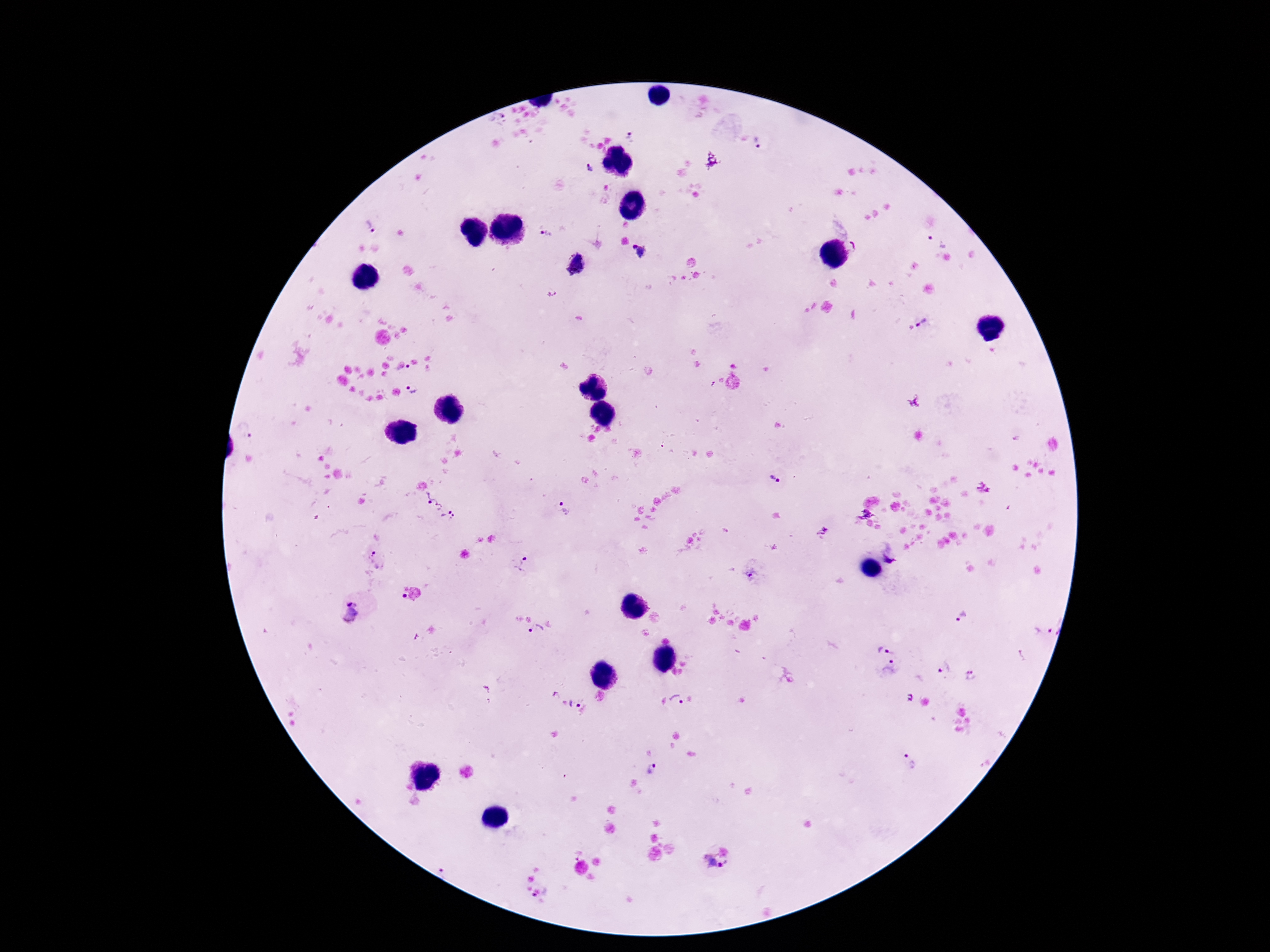

Approximate object centers, in pixels from the top-left corner. Plasmodium parasite locations: (x=632, y=136), (x=759, y=143), (x=590, y=167), (x=371, y=226), (x=546, y=233), (x=938, y=241), (x=855, y=246), (x=643, y=252), (x=575, y=264), (x=922, y=321), (x=409, y=366), (x=413, y=391), (x=247, y=429), (x=775, y=480), (x=435, y=501), (x=563, y=510), (x=449, y=518), (x=822, y=530), (x=378, y=559), (x=524, y=565), (x=751, y=574), (x=403, y=595), (x=351, y=612), (x=962, y=616), (x=536, y=630), (x=1042, y=631), (x=885, y=646), (x=943, y=667), (x=891, y=669), (x=969, y=675), (x=555, y=695), (x=677, y=699), (x=575, y=704), (x=909, y=760), (x=652, y=769), (x=711, y=865), (x=444, y=867), (x=533, y=897). Patient malaria status: infected. Single field of view. Photographed through the microscope eyepiece with a smartphone camera. 100x magnification. Image is 1270×952 pixels. Thick blood film. Giemsa stain.